Report the malaria status of this cell.
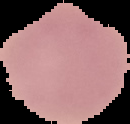

It is uninfected.

Summary:
  - Preparation: thin blood film
  - Image type: segmented cell region with the area outside set to black
  - Image size: 130×124 pixels